State which parasite is depicted.
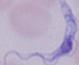

This is a trypanosome.

Photomicrograph. 1000x magnification.